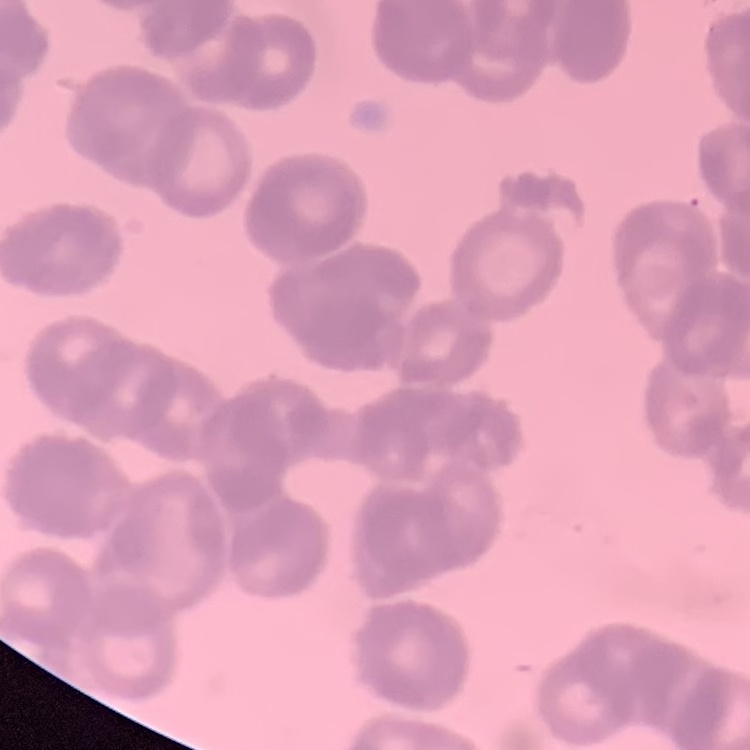
red blood cell morphology = rouleaux formation
preparation = thin peripheral smear
stain = Field's or Giemsa
image type = square crop of a larger photomicrograph